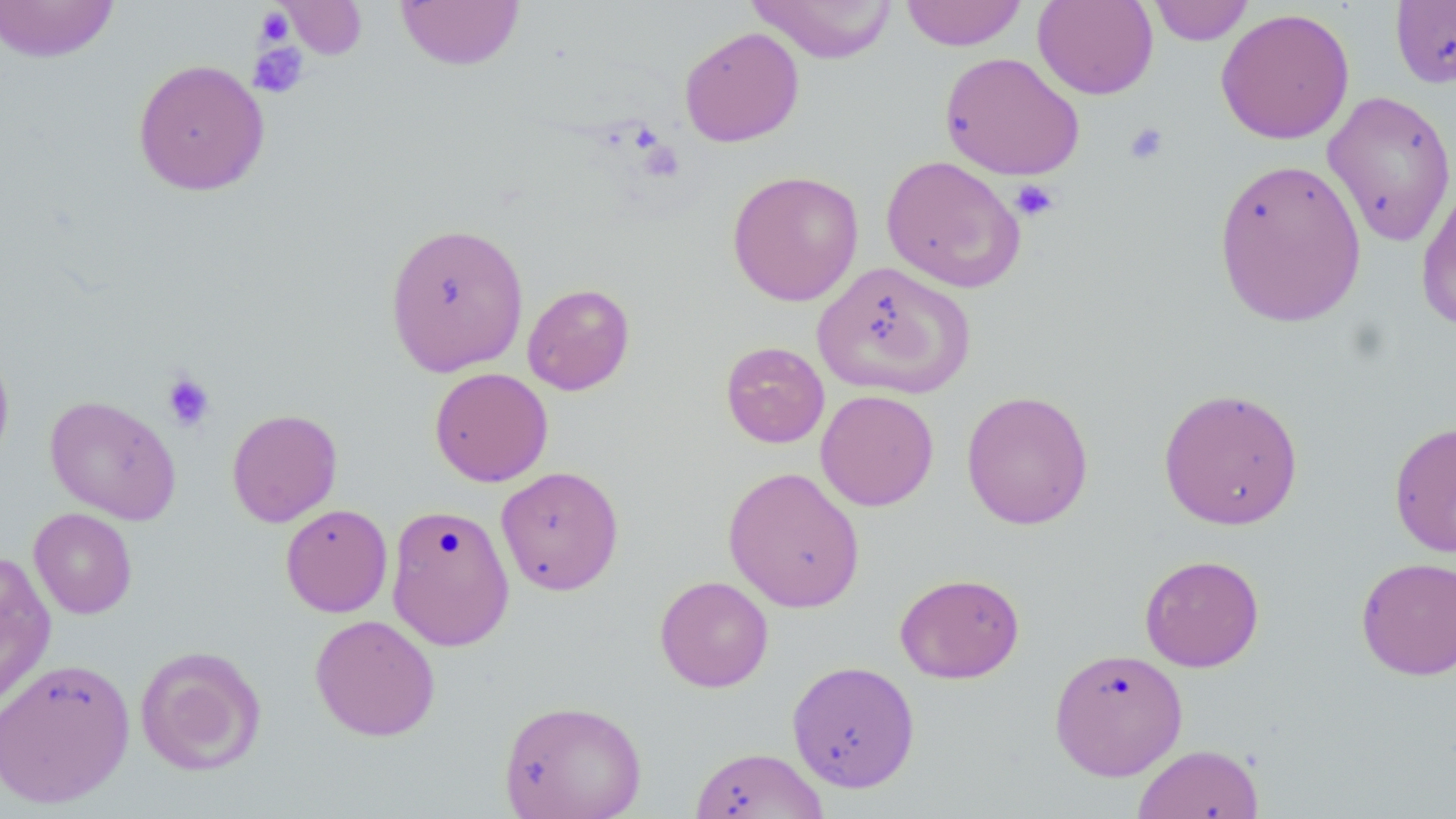
Approximate bounding boxes as (x1,y1)-(x2,y2) corner pairs in pixels. Uninfected red blood cell locations: (0,0)-(121,63), (277,0)-(367,60), (746,0)-(900,63), (900,0)-(1027,51), (1033,0)-(1159,100), (1147,0)-(1254,46), (1390,0)-(1456,89), (396,1)-(525,70), (1215,7)-(1355,144), (679,27)-(804,147), (940,51)-(1085,180), (132,58)-(270,196), (1322,89)-(1456,247), (880,155)-(1026,293), (1212,157)-(1366,328), (726,169)-(864,306), (1415,180)-(1456,334), (384,221)-(530,376), (813,261)-(975,399), (522,283)-(635,396), (720,341)-(830,449), (0,344)-(14,471), (429,367)-(554,487), (1158,387)-(1305,530), (815,389)-(939,511), (961,389)-(1094,530), (44,395)-(182,524), (227,408)-(342,527), (1389,420)-(1456,558), (495,466)-(624,595), (722,466)-(865,613), (280,503)-(393,617), (386,503)-(515,652), (28,508)-(137,619), (0,550)-(56,713), (1140,554)-(1264,672), (1356,556)-(1456,680), (894,572)-(1025,683), (655,575)-(774,692), (310,614)-(440,741), (135,645)-(267,776), (1049,647)-(1188,781), (0,657)-(136,808), (786,660)-(921,793), (498,699)-(647,819), (1132,743)-(1265,819), (689,746)-(830,819). Platelet locations: (255,7)-(294,47), (248,43)-(309,98), (1124,122)-(1169,166), (1010,179)-(1059,222), (161,372)-(215,432). Slide-level diagnosis: no evidence of blood parasites. 1000x magnification. May-Grünwald-Giemsa-stained preparation. Thin blood smear. Image is 1456×819 pixels. Optical microscopy. One field of a larger specimen.